Identify the parasite.
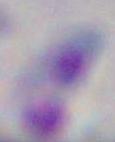
This is Toxoplasma gondii.

Micrograph. 1000x magnification.